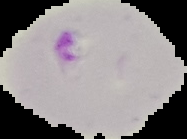 Image is 187×139 pixels. Segmented cell region on a black background. Result: Plasmodium parasites detected. From a thin blood smear.